Classify this cell by malaria status.
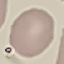
It is uninfected.

{
  "preparation": "thin blood smear",
  "image_type": "automatically extracted cell patch, resized to 64 × 64 pixels",
  "stain": "Giemsa",
  "capture": "smartphone camera at the microscope eyepiece"
}